Assess for malaria.
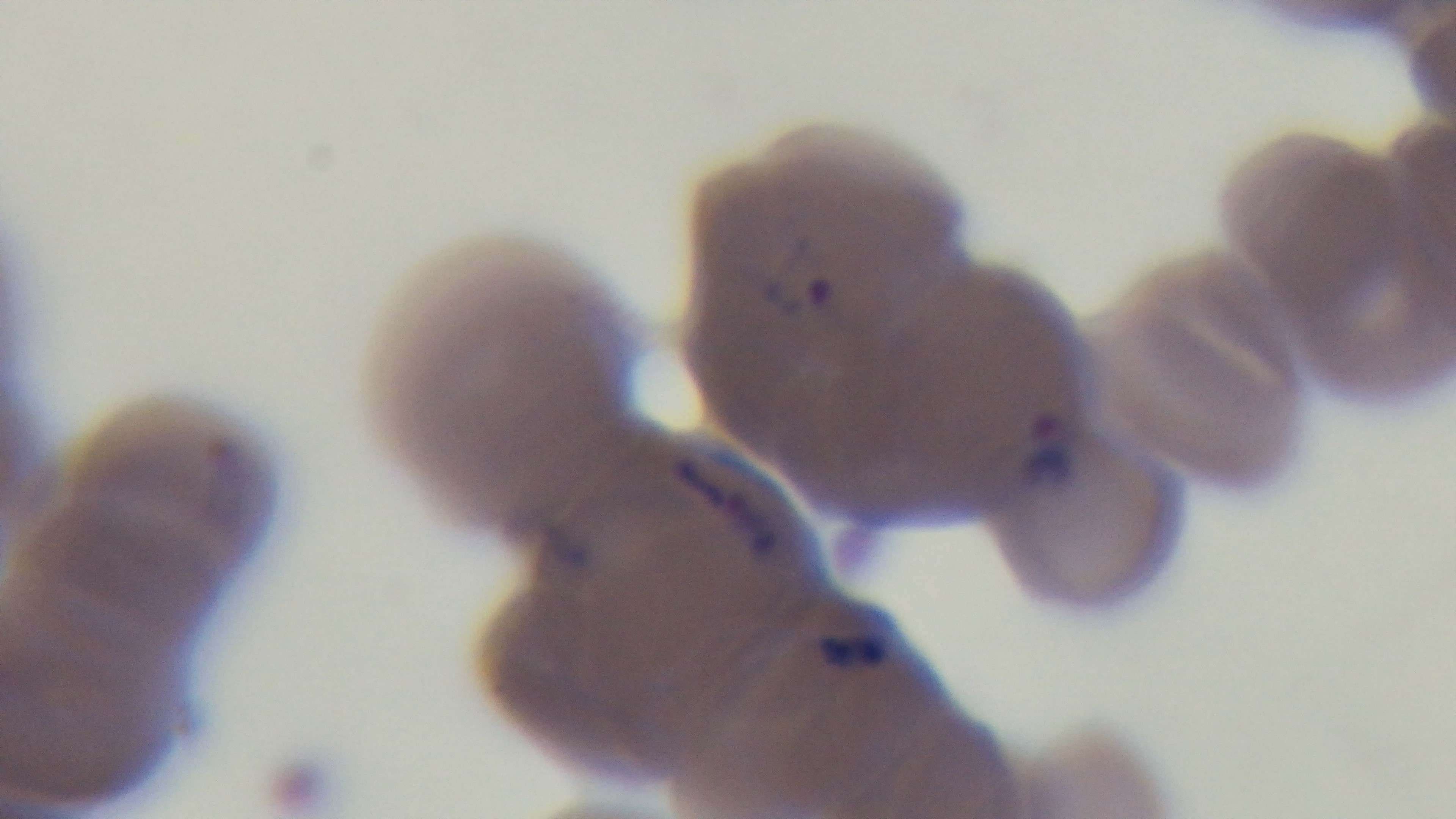
Positive.

Summary:
  - Capture: mounted 4K digital camera
  - Field of view: single
  - Objective: 100x oil immersion
  - Modality: light microscopy
  - Stain: Giemsa
  - Preparation: thin smear